Give the extent of all Plasmodium falciparum-infected red blood cells.
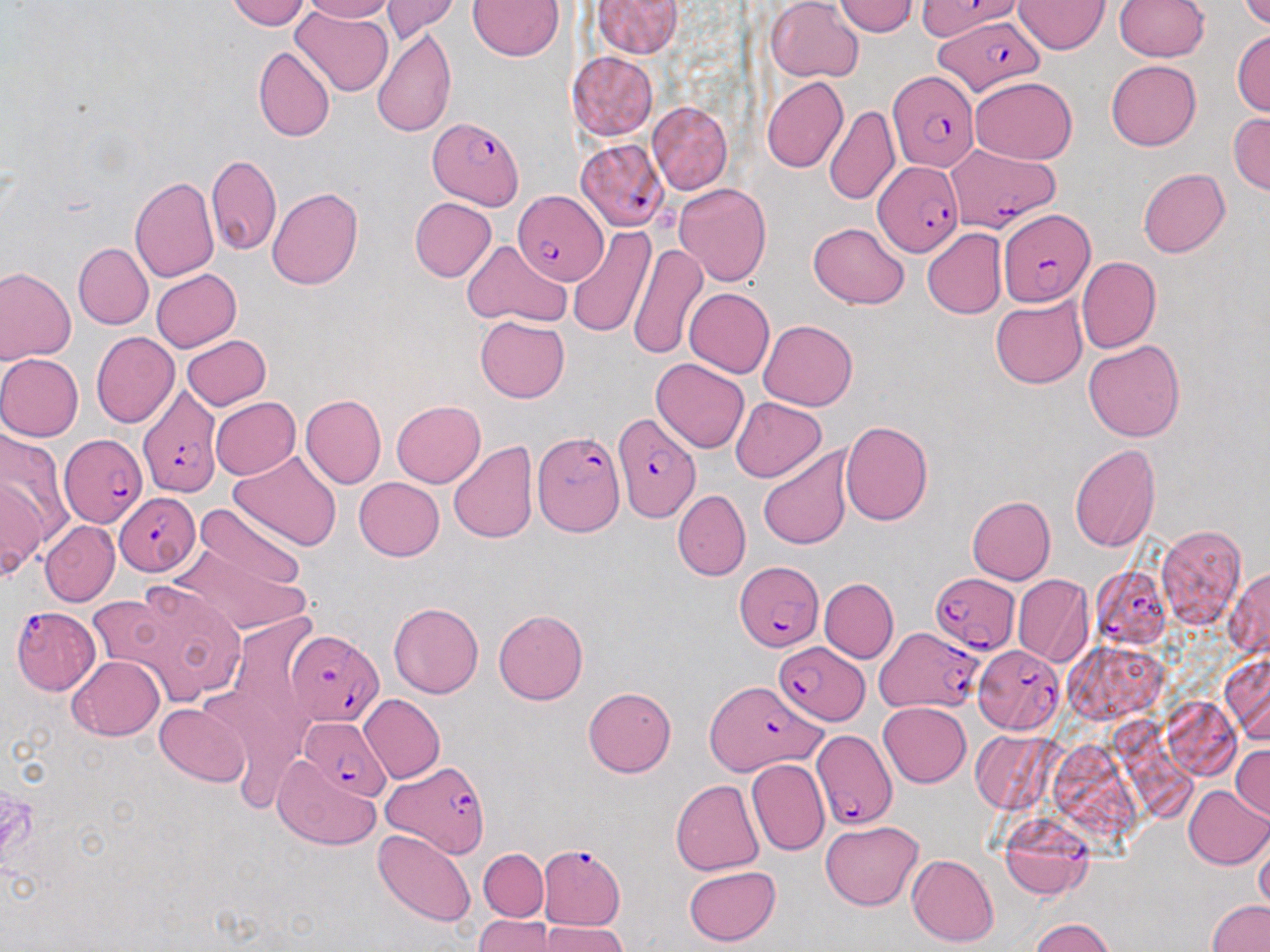
Approximate bounding boxes as (x1,y1)-(x2,y2) corner pairs in pixels.
Plasmodium falciparum-infected red blood cells: (917,0)-(1018,41), (940,15)-(1042,97), (889,69)-(979,172), (428,116)-(525,209), (947,142)-(1055,232), (575,144)-(669,234), (873,162)-(962,259), (512,190)-(609,285), (996,208)-(1096,307), (137,384)-(223,498), (612,410)-(700,522), (532,431)-(623,536), (59,434)-(147,528), (114,491)-(201,574), (736,560)-(822,652), (1091,566)-(1171,649), (930,573)-(1020,653), (11,605)-(98,695), (286,627)-(383,726), (873,627)-(984,713), (773,642)-(870,725), (973,645)-(1065,733), (704,679)-(824,777), (298,720)-(390,800), (810,729)-(896,833), (384,760)-(489,859), (1001,817)-(1093,900), (538,844)-(627,932).

slide-level diagnosis = Plasmodium falciparum
image size = 1270×952 pixels
stain = May-Grünwald-Giemsa
preparation = thin blood film
modality = light microscopy
magnification = 1000x
field of view = one of a larger specimen
uninfected red blood cell locations = approximate bounding boxes as (x1,y1)-(x2,y2) corner pairs in pixels: (225,0)-(309,30), (301,0)-(396,23), (381,0)-(460,41), (592,0)-(685,58), (1015,0)-(1110,55), (1115,0)-(1209,60), (1237,0)-(1270,29), (468,1)-(565,60), (768,1)-(863,83), (834,1)-(918,36), (290,7)-(393,97), (372,25)-(457,137), (1231,29)-(1270,117), (253,45)-(334,142), (568,51)-(658,141), (1106,59)-(1201,150), (970,76)-(1078,165), (762,77)-(848,173), (646,101)-(732,194), (825,104)-(900,206), (1228,112)-(1270,194), (206,153)-(281,258), (210,166)-(338,274), (1138,168)-(1231,257), (129,176)-(221,282), (674,182)-(772,287), (268,188)-(363,289), (410,197)-(496,281), (807,222)-(910,308), (566,224)-(655,339), (922,229)-(1007,319), (461,239)-(571,326), (629,241)-(709,361), (74,242)-(153,329), (1076,257)-(1160,353), (0,266)-(76,364), (152,270)-(240,352), (670,288)-(765,450), (684,288)-(774,377), (991,295)-(1087,389), (475,315)-(569,403), (759,319)-(857,411), (91,330)-(179,428), (182,335)-(271,410), (1083,338)-(1185,442), (0,354)-(84,441), (652,358)-(749,453), (300,394)-(385,489), (210,397)-(301,479), (730,397)-(827,482), (391,400)-(486,488), (841,421)-(933,526), (0,429)-(72,549), (448,440)-(538,544), (1070,443)-(1162,554), (758,446)-(853,549), (229,450)-(342,552), (354,477)-(445,561), (0,479)-(43,582), (672,490)-(750,581), (966,496)-(1055,584), (194,500)-(306,595), (40,521)-(119,606), (1156,525)-(1245,629), (169,535)-(310,637), (1225,568)-(1270,660), (1012,575)-(1093,667), (120,578)-(247,703), (820,578)-(898,663), (86,592)-(177,680), (388,601)-(484,699), (494,610)-(589,705), (1222,652)-(1270,743), (68,656)-(164,740), (583,687)-(677,777), (359,693)-(444,783), (879,701)-(971,787), (156,703)-(248,785), (969,730)-(1057,814), (1231,745)-(1269,819), (271,754)-(381,850), (747,759)-(829,857), (671,779)-(764,876), (1182,786)-(1269,869), (820,819)-(925,911), (374,829)-(475,927), (1254,830)-(1270,915), (478,848)-(548,920), (908,855)-(999,946), (683,865)-(780,946), (1207,900)-(1270,952), (475,914)-(558,951), (1029,918)-(1117,952), (536,920)-(627,952)